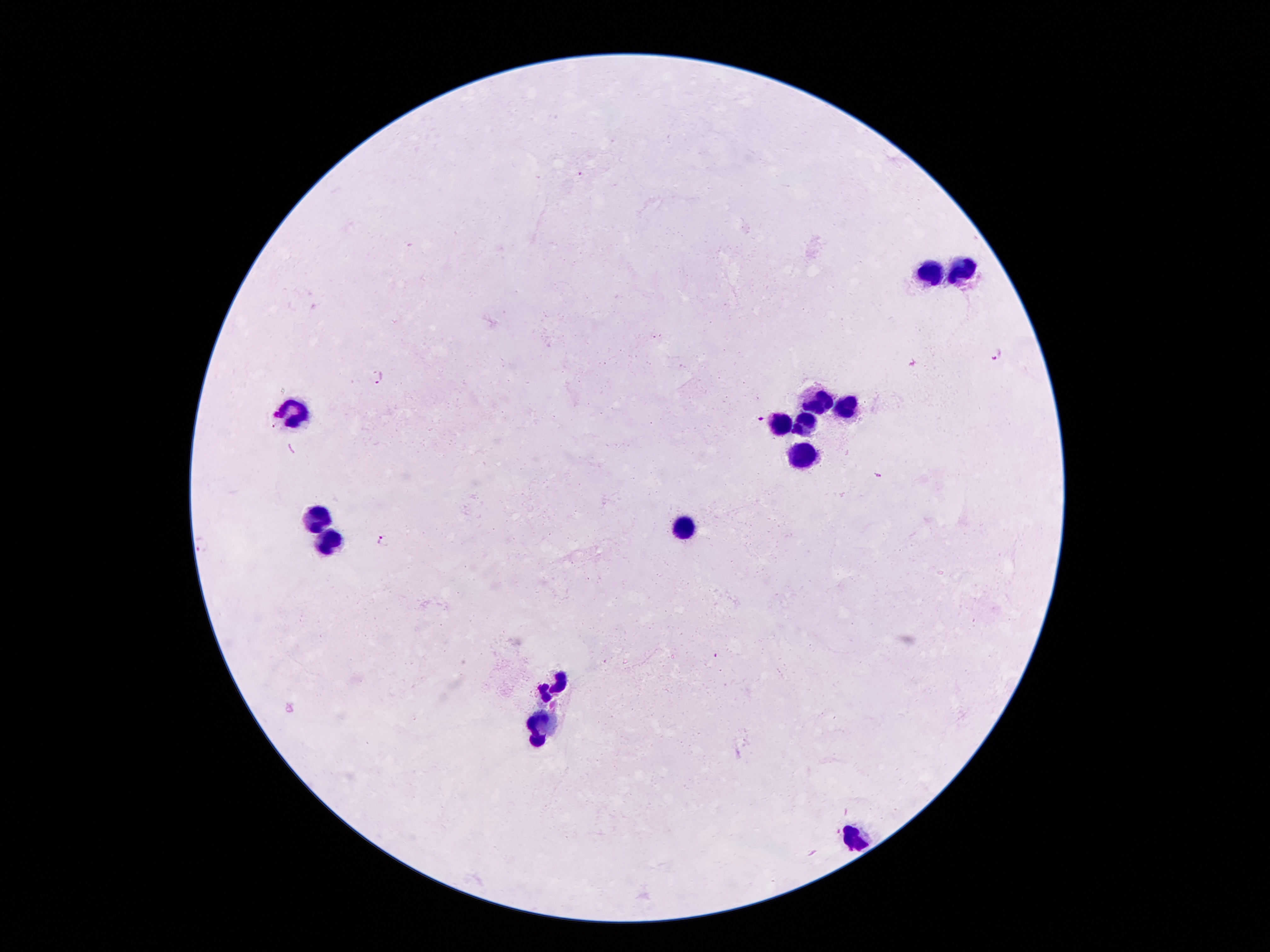
Approximate centers as [x, y] in pixels.
Summary:
  - Leukocyte locations: [928, 274], [966, 275], [821, 396], [847, 407], [292, 410], [783, 424], [806, 425], [801, 453], [317, 516], [686, 527], [330, 544], [551, 685], [541, 725], [857, 837]
  - Malaria parasite locations: [996, 354], [380, 375], [761, 420], [878, 475], [382, 541]
  - Capture: smartphone through the microscope eyepiece
  - Image size: 1270×952 pixels
  - Field of view: single
  - Stain: Giemsa
  - Preparation: thick peripheral-blood smear
  - Patient malaria status: infected with Plasmodium falciparum
  - Magnification: 100x